State the blood parasite species.
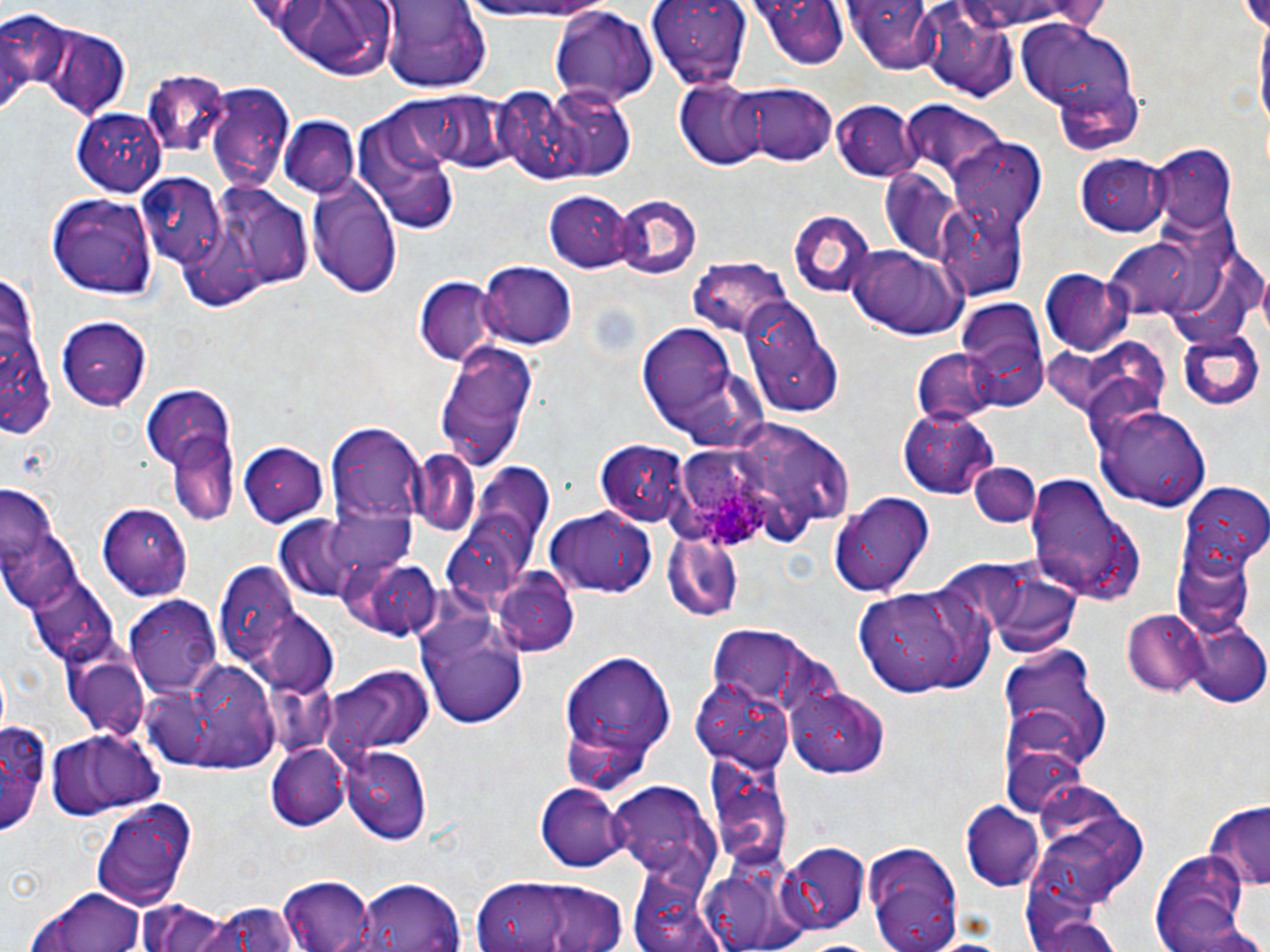
Plasmodium ovale.

image size = 1270×952 pixels
Plasmodium ovale-infected red blood cell locations = approximate bounding boxes as (x1,y1)-(x2,y2) corner pairs in pixels: (687,472)-(769,550)
stain = May-Grünwald-Giemsa
uninfected red blood cell locations = approximate bounding boxes as (x1,y1)-(x2,y2) corner pairs in pixels: (649,0)-(754,89), (847,0)-(945,73), (947,1)-(1104,34), (449,2)-(619,29), (759,2)-(846,71), (381,3)-(488,90), (246,4)-(405,76), (549,6)-(658,103), (921,7)-(1017,100), (0,11)-(67,98), (1018,18)-(1137,117), (36,24)-(130,119), (141,72)-(229,155), (1050,78)-(1143,156), (676,81)-(768,169), (728,82)-(837,166), (207,84)-(293,195), (511,86)-(639,185), (422,93)-(513,173), (905,98)-(1006,174), (831,99)-(919,180), (73,106)-(168,193), (354,109)-(461,235), (278,118)-(359,196), (951,137)-(1048,230), (1150,144)-(1237,235), (1075,152)-(1169,236), (135,172)-(228,269), (880,172)-(972,261), (306,175)-(402,298), (215,185)-(314,290), (44,190)-(158,299), (549,190)-(634,276), (612,193)-(704,280), (935,199)-(1032,301), (786,209)-(876,297), (184,225)-(263,315), (1105,232)-(1211,319), (844,244)-(969,342), (690,259)-(791,339), (479,263)-(579,348), (1,264)-(51,442), (1041,270)-(1132,355), (416,276)-(498,365), (743,301)-(843,419), (952,305)-(1049,409), (56,313)-(150,410), (636,320)-(755,448), (1179,330)-(1263,411), (433,339)-(536,472), (1083,342)-(1177,410), (912,348)-(1003,427), (144,386)-(238,486), (1093,402)-(1210,513), (900,407)-(997,497), (733,419)-(831,496), (327,422)-(425,528), (172,433)-(238,524), (597,440)-(691,526), (239,443)-(326,527), (781,446)-(854,522), (419,453)-(477,535), (471,461)-(559,546), (967,462)-(1042,531), (1026,474)-(1145,604), (1182,484)-(1270,565), (1,489)-(80,620), (826,490)-(935,597), (100,502)-(193,599), (547,508)-(656,599), (320,513)-(415,585), (661,530)-(745,624), (445,531)-(530,619), (1170,546)-(1255,637), (341,556)-(442,641), (204,560)-(322,686), (976,561)-(1083,654), (494,572)-(579,656), (25,576)-(120,668), (855,581)-(992,698), (125,595)-(222,694), (1122,610)-(1206,696), (417,611)-(528,732), (1182,620)-(1268,708), (708,627)-(808,701), (996,646)-(1111,766), (555,649)-(680,790), (62,653)-(150,741), (146,655)-(283,774), (324,666)-(431,758), (692,677)-(793,767), (258,681)-(348,757), (788,686)-(888,775), (1,710)-(55,834), (46,730)-(161,819), (999,736)-(1087,819), (268,743)-(348,828), (342,745)-(432,844), (610,782)-(714,883), (535,783)-(630,873), (89,797)-(195,909), (962,802)-(1045,891), (1202,804)-(1270,895), (1042,832)-(1127,908), (863,842)-(964,952), (779,843)-(870,933), (1150,849)-(1252,952), (700,862)-(804,952), (279,872)-(377,950), (625,872)-(726,952), (468,874)-(630,952), (356,880)-(467,952), (27,887)-(152,952), (195,899)-(301,952), (137,900)-(233,952), (1027,905)-(1125,952), (791,937)-(887,951)
preparation = thin blood film
field of view = single
modality = light microscopy
magnification = 1000x